Report the malaria status of this cell.
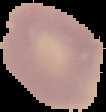
Uninfected.

Segmented cell region on a black background. Image is 106×112 pixels. From a thin blood smear.